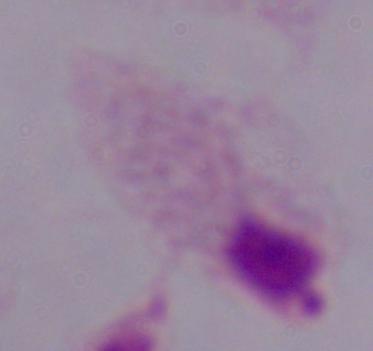 Micrograph. Captured at 1000x magnification. A trichomonad is seen.